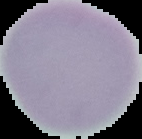 From a thin blood smear. The area outside the segmented cell region is set to black. Image is 142×139 pixels. Malaria status: uninfected.